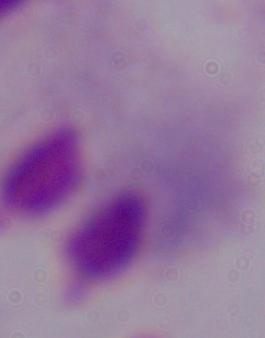 1000x magnification. A trichomonad is seen. Micrograph.